Identify the parasite.
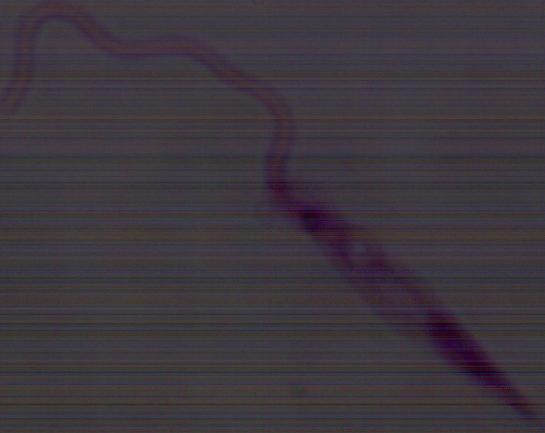
This is Leishmania.

Micrograph. Captured at 1000x magnification.